Report the malaria status of this cell.
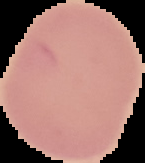
It is uninfected.

Summary:
  - Image size: 145×163 pixels
  - Image type: segmented cell region with the area outside set to black
  - Preparation: thin blood film